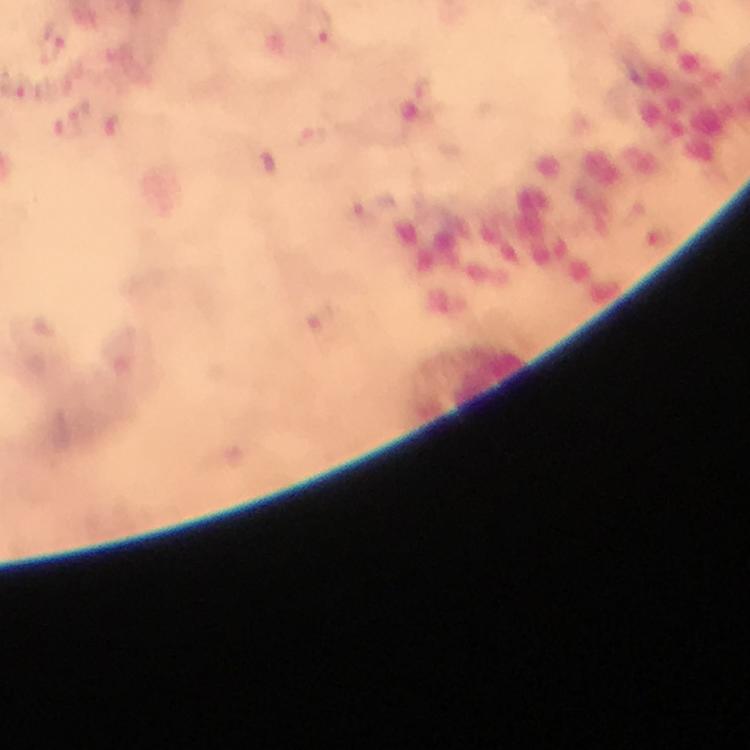

immersion oil = used
stain = Giemsa
Plasmodium parasite locations = approximate object centers, in pixels from the top-left corner: (x=320, y=30), (x=51, y=45), (x=67, y=127), (x=120, y=130), (x=315, y=138), (x=362, y=212)
context = from a malaria diagnostic workup
cropped from = one field of view
magnification = 100x
capture = smartphone mounted on the microscope
preparation = thick blood smear
image size = 750×750 pixels